Give the position of every Plasmodium parasite visible.
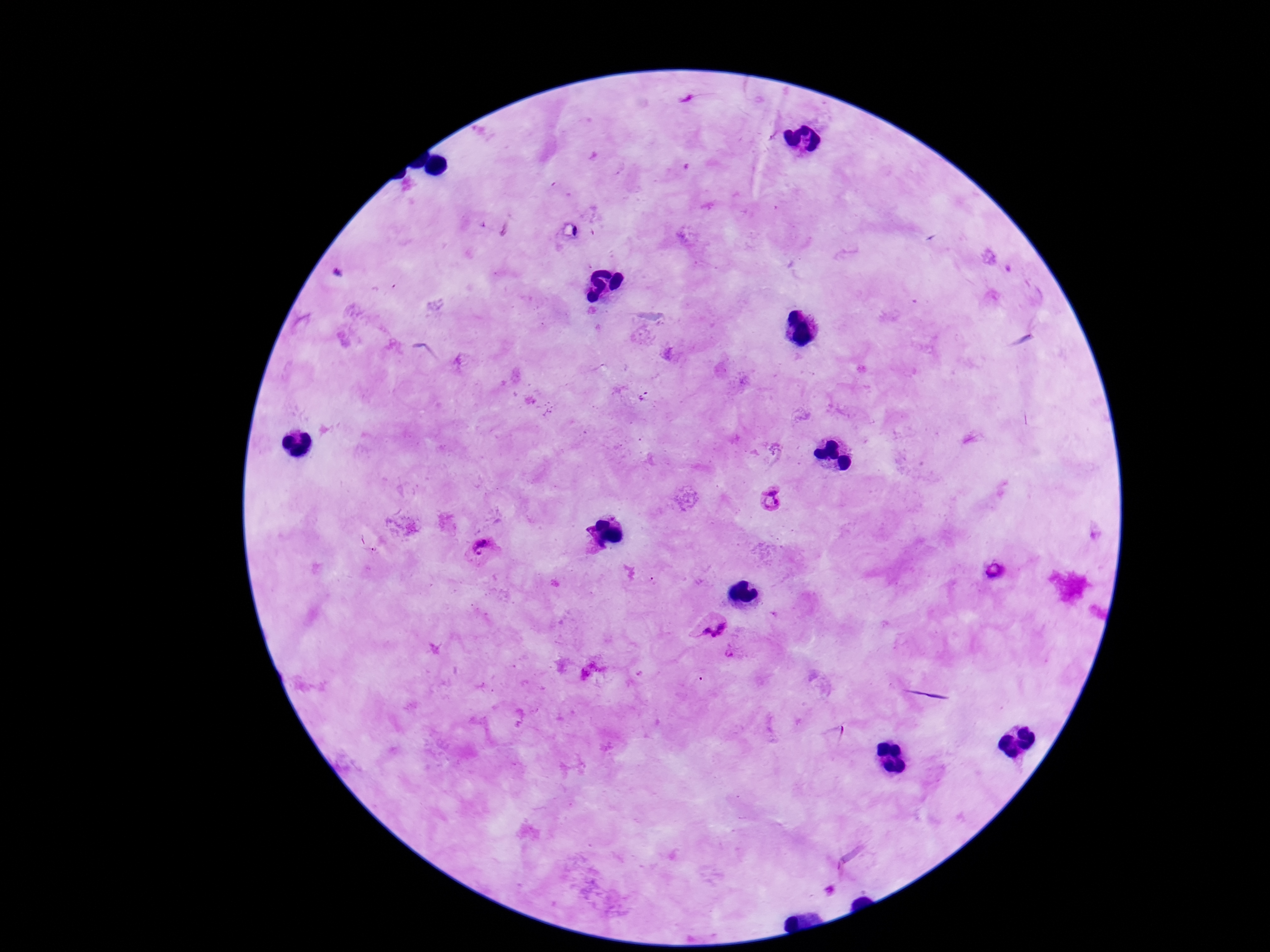

Approximate centers as [x, y] in pixels.
Plasmodium parasites: [771, 497], [588, 541], [481, 549], [996, 573], [712, 622], [729, 654].

stain = Giemsa
preparation = thick blood smear
magnification = 100x
capture = smartphone camera through the microscope eyepiece
field of view = single
patient malaria status = infected
image size = 1270×952 pixels